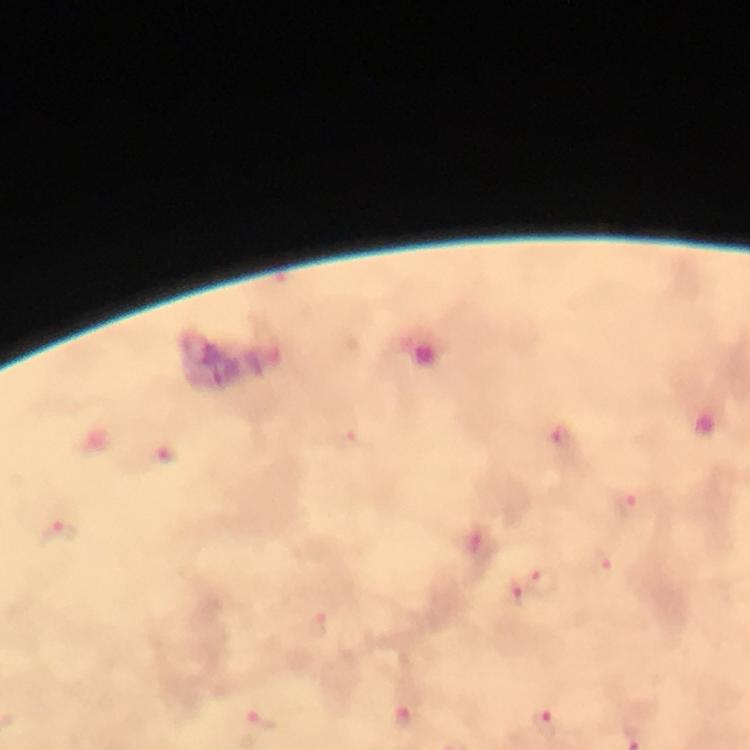
magnification = 100x
stain = Giemsa
immersion oil = used
preparation = thick blood film
malaria parasite locations = approximate centers as {x, y} in pixels: {563, 439}, {629, 504}, {59, 532}, {544, 582}, {318, 625}, {406, 717}, {263, 720}, {545, 724}
context = from a diagnostic examination for malaria
image size = 750×750 pixels
cropped from = a single field of view
capture = smartphone mounted on the microscope